Assess this cell for malaria.
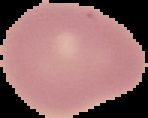

Uninfected.

Summary:
  - Image type: cell region segmented out of the field of view; surrounding area masked to black
  - Preparation: thin blood smear
  - Image size: 148×118 pixels